Report the malaria status of this cell.
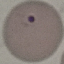
It is uninfected.

capture = smartphone camera at the microscope eyepiece
preparation = thin blood film
image type = cell patch, automatically extracted from a larger field of view and resized to 64 × 64 pixels
stain = Giemsa